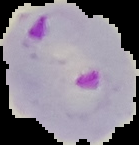

Image is 139×145 pixels. From a thin blood film. Result: malaria parasites identified. Segmented cell region on a black background.